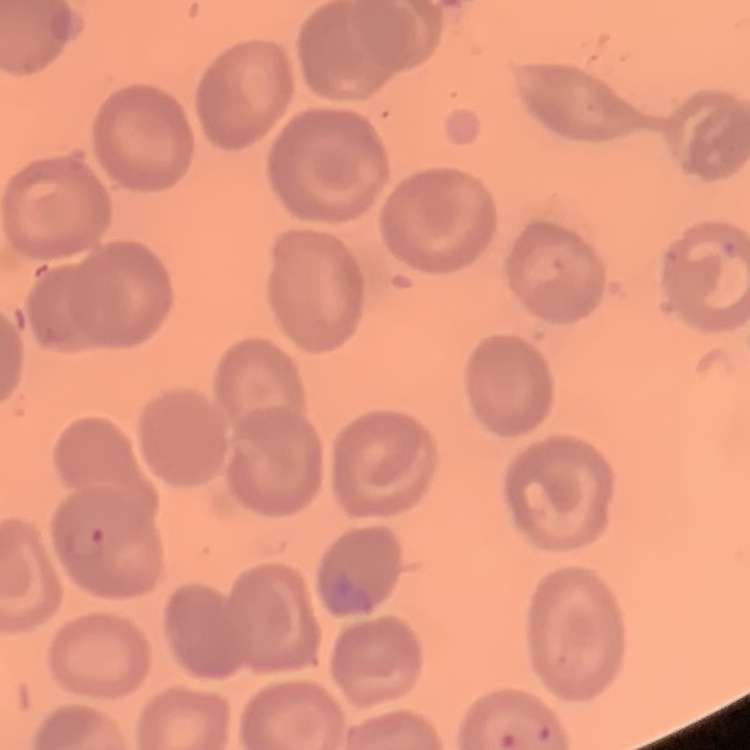
{
  "erythrocyte_morphology": "no rouleaux formation",
  "image_type": "square crop of a larger photomicrograph",
  "preparation": "thin peripheral smear",
  "stain": "Field's or Giemsa"
}